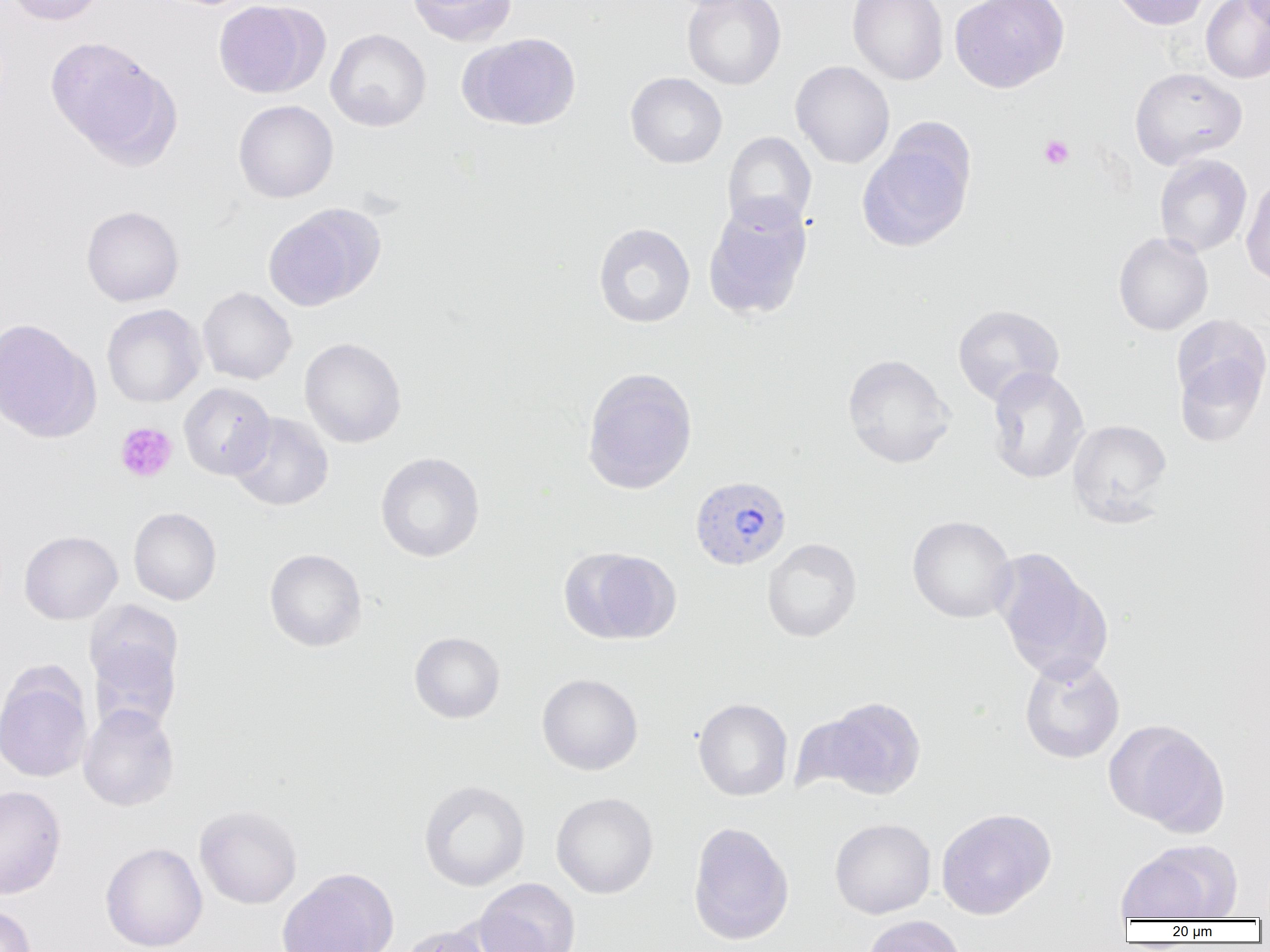
slide-level diagnosis = Plasmodium vivax
magnification = 1000x
Plasmodium vivax-infected red blood cell locations = approximate bounding boxes as [x1, y1, x2, y2] in pixels: [689, 475, 792, 571]
preparation = thin blood film
modality = light microscopy
image size = 1270×952 pixels
uninfected red blood cell locations = approximate bounding boxes as [x1, y1, x2, y2] in pixels: [5, 0, 109, 26], [213, 0, 324, 99], [406, 0, 517, 46], [682, 0, 787, 90], [848, 0, 949, 85], [949, 0, 1069, 93], [1111, 0, 1211, 30], [1201, 0, 1270, 83], [1240, 0, 1270, 32], [325, 28, 431, 132], [461, 32, 582, 131], [46, 36, 179, 165], [790, 60, 895, 168], [1129, 67, 1247, 169], [625, 71, 728, 169], [233, 99, 339, 203], [857, 129, 975, 252], [722, 131, 817, 233], [1154, 154, 1252, 257], [1240, 176, 1270, 287], [703, 197, 813, 321], [263, 204, 384, 311], [81, 206, 184, 307], [593, 222, 695, 328], [1113, 232, 1213, 336], [197, 287, 297, 385], [101, 304, 206, 408], [952, 304, 1065, 406], [1171, 314, 1270, 432], [0, 318, 99, 442], [299, 337, 407, 448], [842, 353, 955, 469], [986, 366, 1090, 485], [581, 367, 698, 494], [178, 383, 276, 480], [229, 412, 333, 512], [1068, 419, 1172, 525], [375, 452, 485, 562], [128, 507, 222, 605], [907, 515, 1017, 623], [19, 530, 122, 624], [762, 538, 862, 642], [561, 547, 681, 645], [264, 548, 367, 652], [991, 548, 1111, 682], [87, 624, 183, 734], [409, 631, 505, 723], [1019, 654, 1125, 763], [0, 665, 93, 783], [537, 673, 643, 775], [807, 696, 928, 800], [693, 698, 793, 801], [78, 703, 180, 812], [1104, 718, 1228, 833], [418, 779, 530, 892], [0, 785, 66, 899], [551, 792, 658, 899], [194, 805, 303, 909], [936, 807, 1056, 919], [829, 818, 936, 919], [687, 821, 795, 946], [1116, 841, 1240, 921], [100, 842, 208, 952], [276, 867, 399, 952], [474, 877, 580, 952], [0, 904, 37, 952], [861, 915, 967, 952], [398, 925, 497, 952]
field of view = single
platelet locations = approximate bounding boxes as [x1, y1, x2, y2] in pixels: [1039, 134, 1074, 169], [115, 422, 177, 483]